Report the malaria status of this cell.
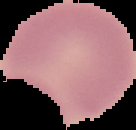

Uninfected.

Summary:
  - Image type: segmented cell region with the area outside set to black
  - Image size: 136×130 pixels
  - Preparation: thin blood smear